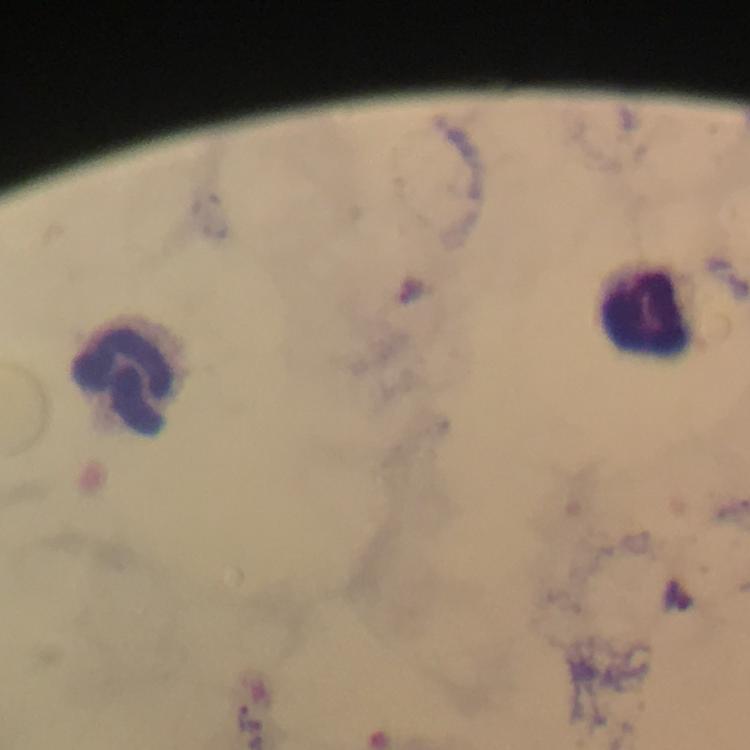
Approximate object centers, in pixels from the top-left corner. Plasmodium parasite locations: (x=412, y=288), (x=254, y=716). Leukocyte locations: (x=643, y=307), (x=123, y=378). Immersion oil was used. From a diagnostic examination for malaria. A crop from one field of view. Image is 750×750 pixels. Giemsa stain. Thick blood film. Photographed through the microscope with a smartphone camera. 100x magnification.